Report the malaria status of this cell.
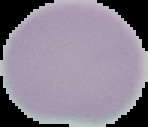
It is uninfected.

{
  "preparation": "thin blood film",
  "image_type": "segmented cell region on a black background",
  "image_size": "148×127 pixels"
}